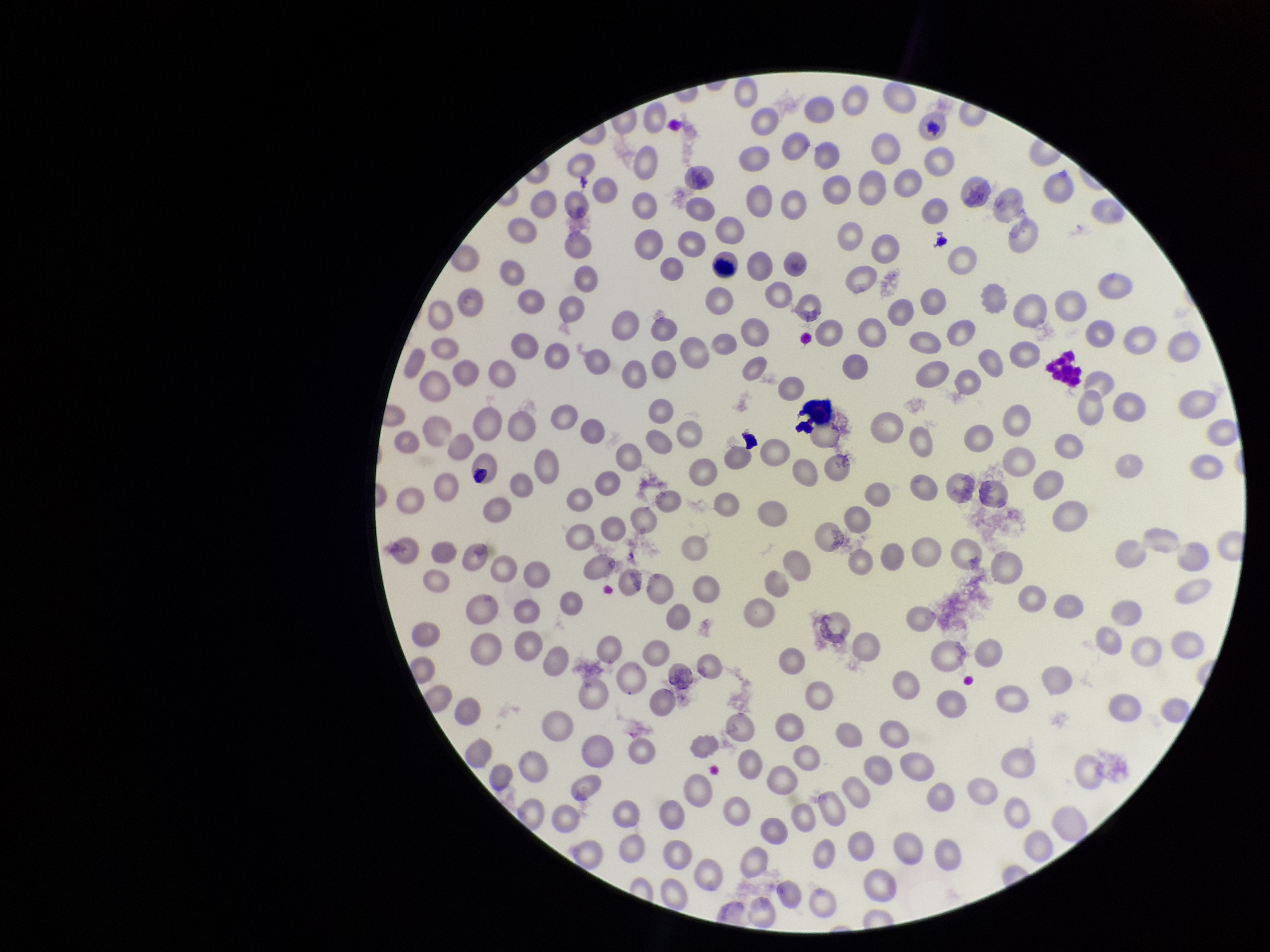
Patient malaria status: positive. Red blood cell count: 233. Parasitized red blood cell count: 0. Species reported for this patient: Plasmodium vivax. Preparation: thin. Single field of view. Parasitized red blood cells: none identified. Stained with Giemsa. Image is 1270×952 pixels. Photographed through the microscope eyepiece with a smartphone camera.